Name the parasite shown.
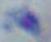

Toxoplasma gondii.

1000x magnification. Micrograph.